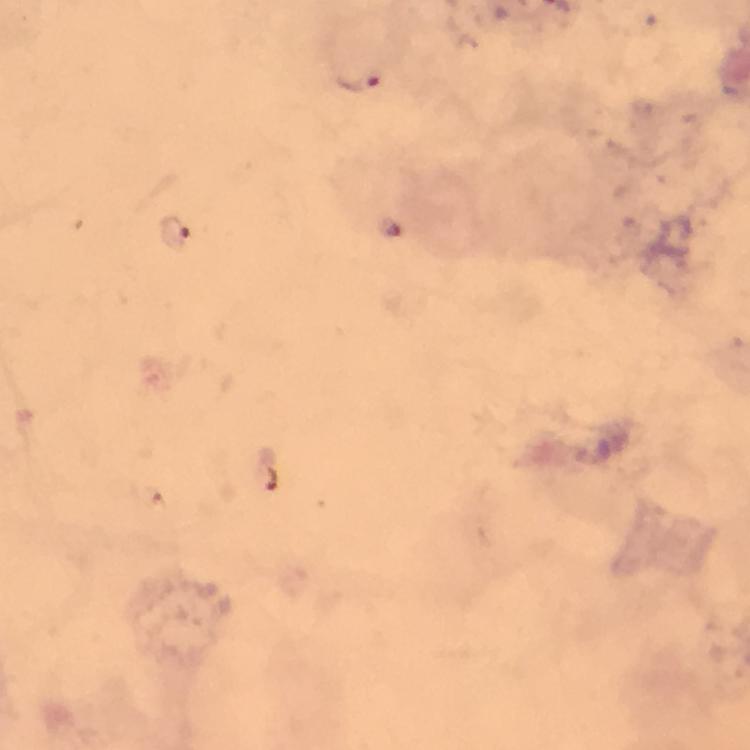
Plasmodium parasite locations = approximate centers as (x, y) in pixels: (352, 80), (176, 234)
context = from a diagnostic examination for malaria
immersion oil = applied
image size = 750×750 pixels
preparation = thick smear
magnification = 100x
cropped from = a single field of view
stain = Giemsa
capture = smartphone camera through the microscope